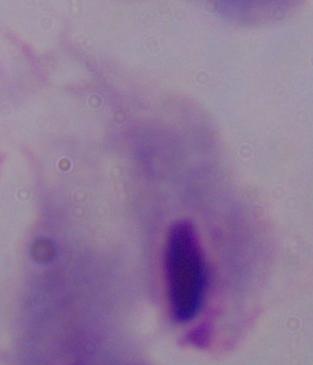

Summary:
  - Identification: trichomonad
  - Magnification: 1000x
  - Modality: micrograph